Classify this cell by malaria status.
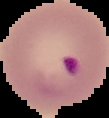
Parasitized.

Summary:
  - Image size: 109×118 pixels
  - Image type: cell region segmented out of the field of view; surrounding area masked to black
  - Preparation: thin blood film